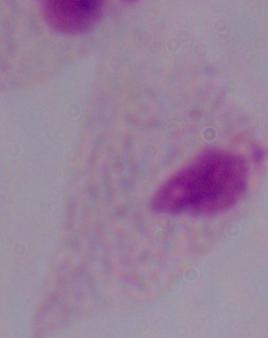
magnification = 1000x
identification = trichomonad
modality = photomicrograph